Evaluate for malaria.
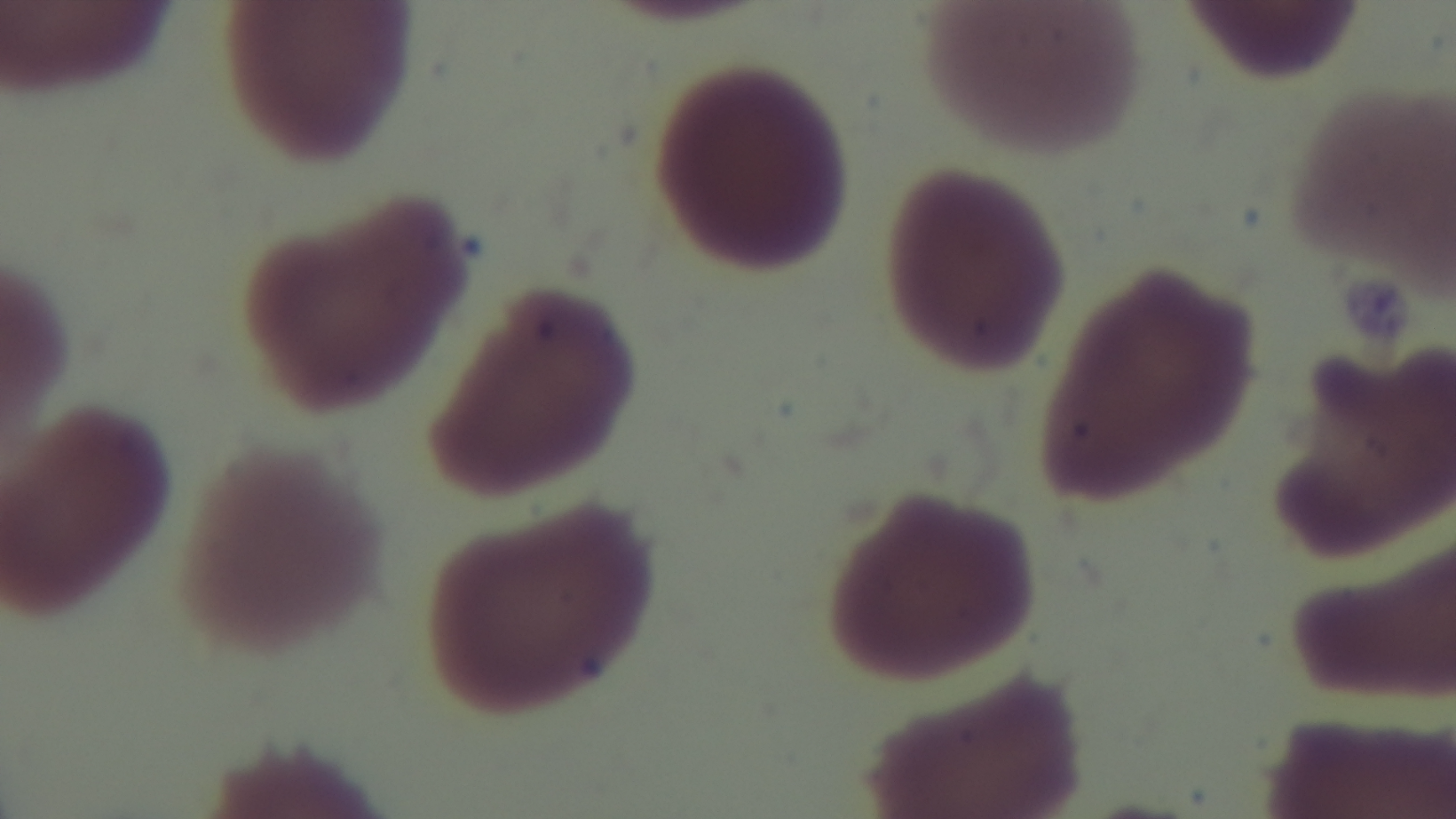
Negative.

modality = light microscopy
objective = 100x oil immersion
preparation = thin
stain = Giemsa
capture = mounted 4K digital camera
field of view = single